Locate every leukocyte (white blood cell).
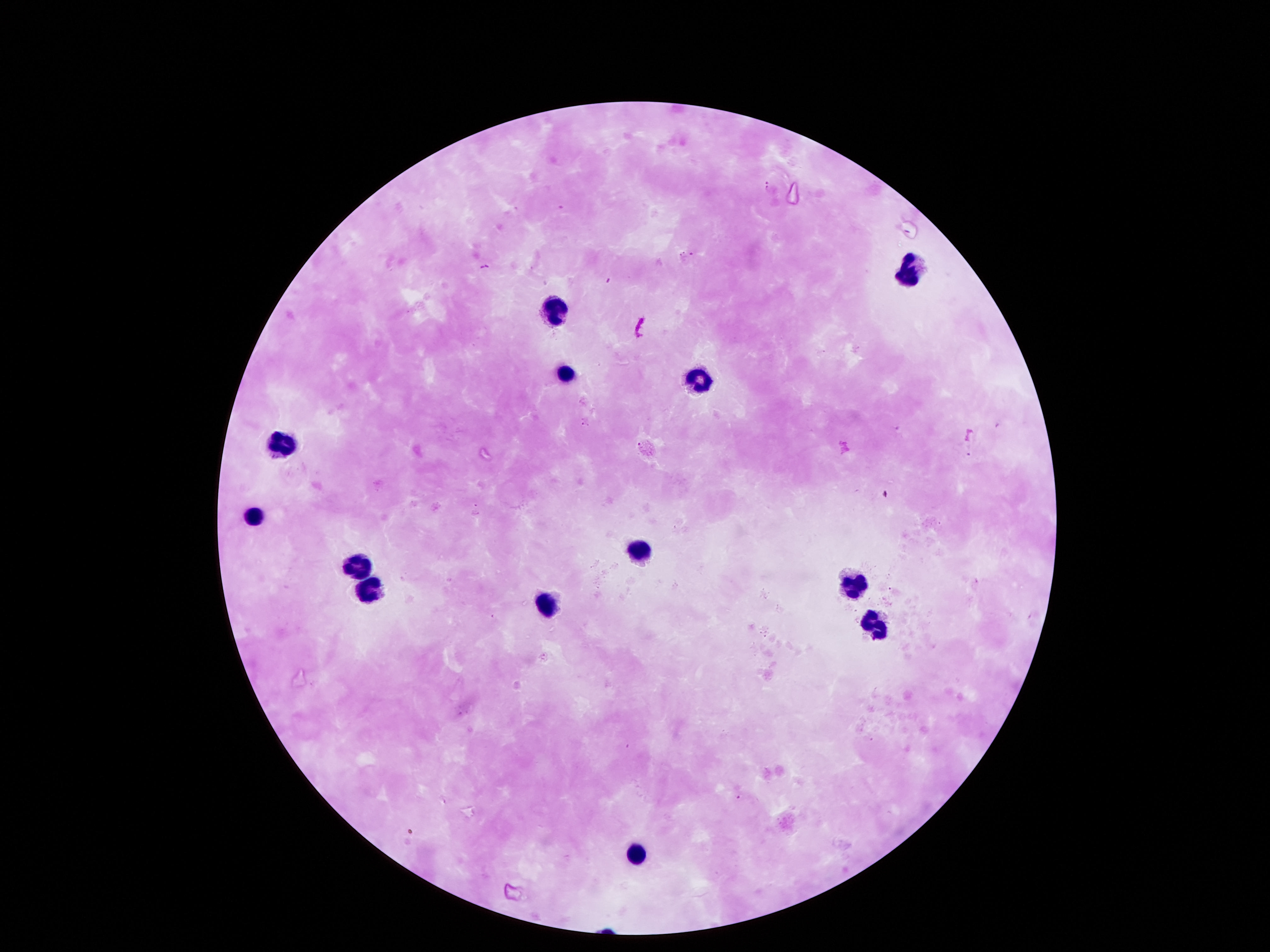

Approximate centers as {x, y} in pixels.
Leukocytes: {907, 269}, {548, 308}, {564, 369}, {697, 378}, {283, 437}, {254, 513}, {645, 550}, {358, 562}, {849, 578}, {370, 589}, {551, 598}, {871, 624}, {635, 850}.

Giemsa-stained preparation. Smartphone photograph taken through the microscope eyepiece. Image is 1270×952 pixels. Single field of view. Patient malaria status: negative. 100x magnification. Thick blood film.